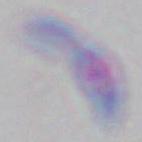
Summary:
  - Identification: Toxoplasma gondii
  - Magnification: 1000x
  - Modality: micrograph